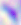
Summary:
  - Modality: micrograph
  - Magnification: 400x
  - Identification: Toxoplasma gondii